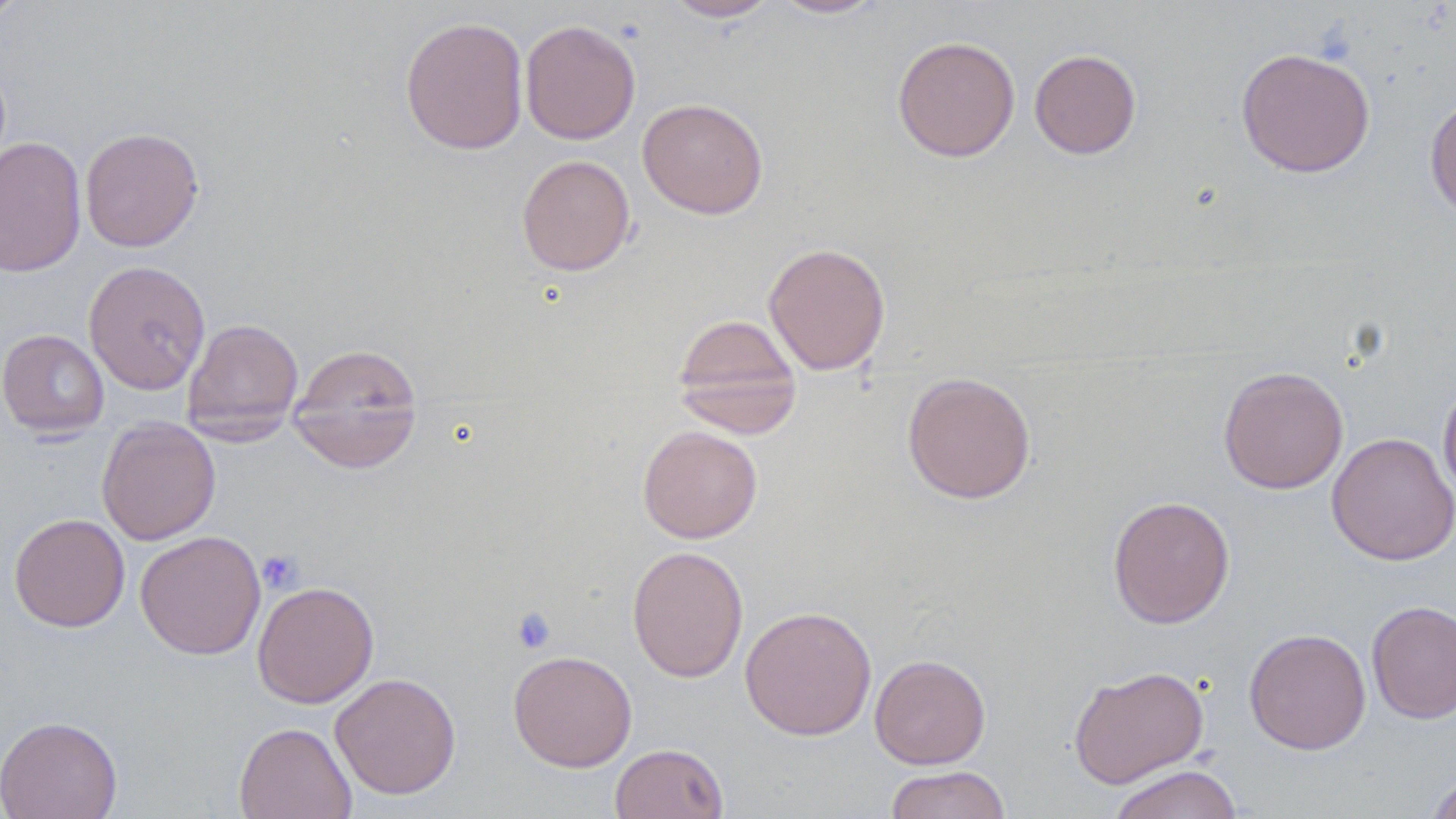
Summary:
  - Coordinate format: approximate bounding boxes as named x1/y1/x2/y2 corners in pixels
  - Platelet locations: (x1=257, y1=550, x2=304, y2=594), (x1=511, y1=605, x2=557, y2=654)
  - Uninfected red blood cell locations: (x1=0, y1=0, x2=28, y2=27), (x1=662, y1=0, x2=779, y2=22), (x1=768, y1=0, x2=886, y2=19), (x1=400, y1=15, x2=529, y2=155), (x1=520, y1=19, x2=641, y2=145), (x1=892, y1=35, x2=1020, y2=162), (x1=1235, y1=47, x2=1375, y2=178), (x1=1029, y1=49, x2=1142, y2=159), (x1=1424, y1=93, x2=1456, y2=223), (x1=637, y1=98, x2=769, y2=219), (x1=80, y1=127, x2=204, y2=253), (x1=0, y1=136, x2=86, y2=277), (x1=516, y1=154, x2=635, y2=276), (x1=763, y1=242, x2=891, y2=376), (x1=83, y1=260, x2=211, y2=395), (x1=671, y1=312, x2=802, y2=438), (x1=183, y1=318, x2=304, y2=434), (x1=0, y1=329, x2=110, y2=438), (x1=287, y1=344, x2=423, y2=473), (x1=1218, y1=365, x2=1348, y2=494), (x1=901, y1=371, x2=1036, y2=505), (x1=1438, y1=378, x2=1456, y2=504), (x1=96, y1=416, x2=221, y2=546), (x1=637, y1=425, x2=763, y2=543), (x1=1327, y1=432, x2=1456, y2=565), (x1=1107, y1=495, x2=1235, y2=628), (x1=8, y1=513, x2=130, y2=633), (x1=135, y1=530, x2=266, y2=659), (x1=626, y1=545, x2=748, y2=682), (x1=252, y1=581, x2=379, y2=708), (x1=1366, y1=600, x2=1456, y2=724), (x1=739, y1=605, x2=877, y2=741), (x1=1243, y1=627, x2=1371, y2=755), (x1=508, y1=650, x2=637, y2=772), (x1=869, y1=653, x2=991, y2=769), (x1=1068, y1=665, x2=1209, y2=788), (x1=329, y1=672, x2=461, y2=799), (x1=0, y1=715, x2=122, y2=819), (x1=233, y1=721, x2=357, y2=819), (x1=609, y1=742, x2=728, y2=819), (x1=1107, y1=764, x2=1245, y2=819), (x1=885, y1=766, x2=1011, y2=819), (x1=1423, y1=772, x2=1456, y2=819)
  - Slide-level diagnosis: no evidence of blood parasites
  - Field of view: single
  - Magnification: 1000x
  - Stain: May-Grünwald-Giemsa
  - Modality: light microscopy
  - Preparation: thin blood film
  - Image size: 1456×819 pixels